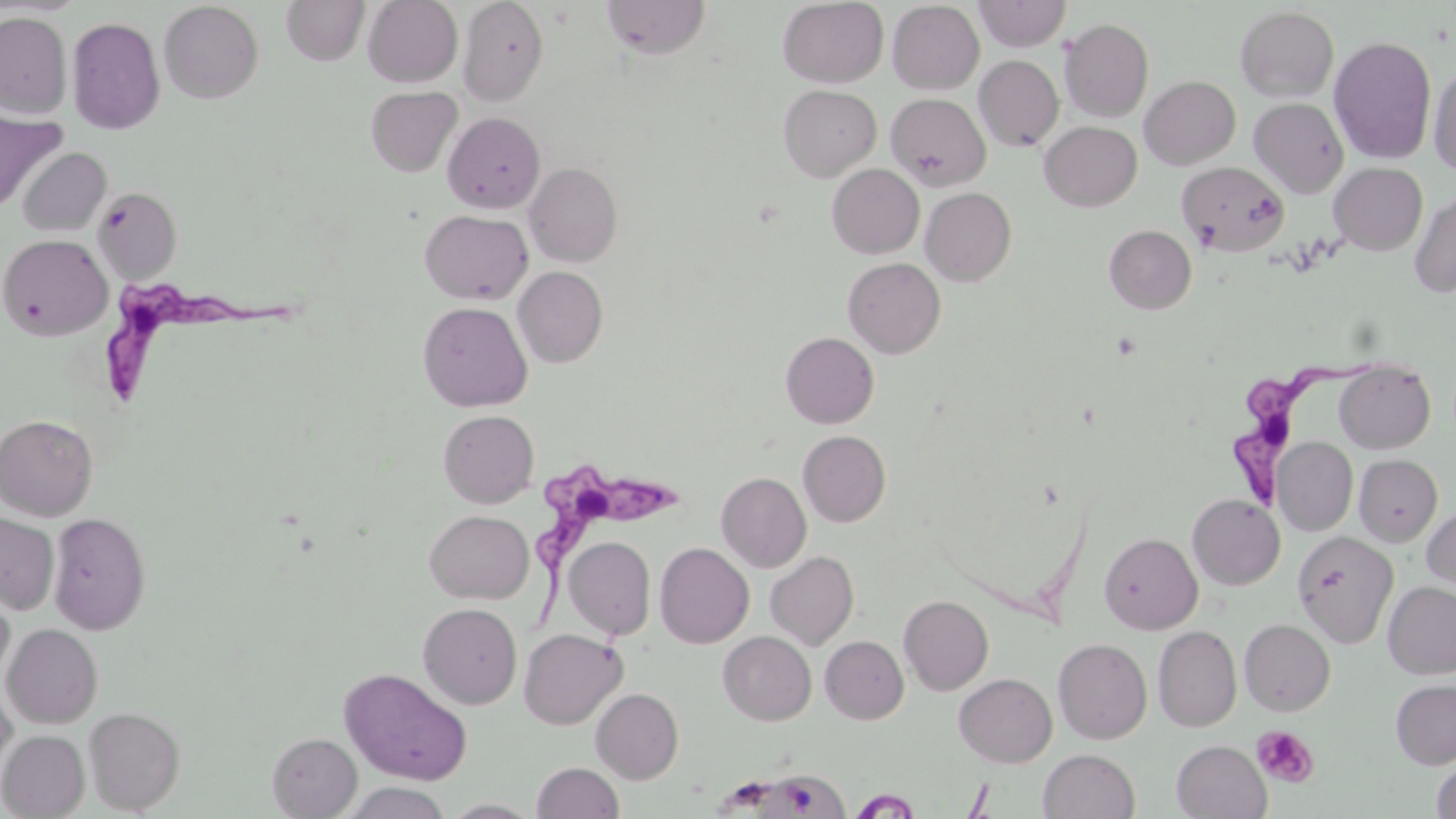
slide-level diagnosis = Trypanosoma brucei
magnification = 1000x
uninfected red blood cell locations = approximate bounding boxes as (x1,y1)-(x2,y2) corner pairs in pixels: (281,0)-(370,66), (363,0)-(463,87), (457,0)-(548,107), (601,0)-(710,59), (777,0)-(889,88), (974,0)-(1071,51), (159,1)-(264,103), (887,1)-(985,94), (1235,5)-(1339,103), (66,10)-(262,118), (0,12)-(72,118), (66,17)-(166,134), (1060,18)-(1154,123), (1328,36)-(1437,164), (974,55)-(1064,152), (1428,61)-(1456,177), (1140,75)-(1240,169), (778,85)-(881,182), (365,86)-(462,177), (886,93)-(991,190), (1249,97)-(1349,198), (0,109)-(66,212), (443,112)-(545,213), (1039,121)-(1142,211), (18,147)-(111,236), (1177,161)-(1289,255), (524,162)-(623,267), (1329,162)-(1428,255), (827,164)-(924,258), (93,187)-(182,282), (921,187)-(1016,286), (1410,189)-(1456,298), (420,210)-(533,304), (1104,225)-(1197,314), (1,233)-(113,340), (843,257)-(945,358), (514,266)-(609,367), (418,301)-(532,412), (781,332)-(879,428), (1334,360)-(1435,454), (438,409)-(539,508), (0,414)-(98,520), (798,430)-(891,527), (1273,437)-(1358,536), (1354,455)-(1443,546), (716,472)-(811,572), (1187,494)-(1285,590), (1422,504)-(1456,595), (424,510)-(534,604), (48,512)-(151,635), (0,514)-(59,614), (1293,531)-(1398,647), (1099,532)-(1203,635), (564,536)-(656,640), (654,542)-(754,648), (765,551)-(859,650), (1383,582)-(1456,679), (0,588)-(15,688), (899,595)-(993,695), (418,603)-(522,709), (1239,619)-(1335,716), (2,624)-(103,728), (1153,626)-(1242,731), (519,628)-(627,729), (718,631)-(816,725), (820,636)-(909,724), (1053,638)-(1152,744), (338,666)-(473,785), (954,673)-(1057,767), (1390,679)-(1456,769), (0,680)-(17,781), (590,688)-(684,784), (84,706)-(185,814), (0,730)-(89,818), (267,732)-(362,818), (1172,740)-(1271,818), (1039,749)-(1140,819), (1431,760)-(1456,818), (532,762)-(623,819), (760,770)-(855,819), (341,782)-(452,819), (849,788)-(923,817), (441,799)-(542,818)
Trypanosoma brucei locations = approximate bounding boxes as (x1,y1)-(x2,y2) corner pairs in pixels: (106,271)-(311,403), (1224,352)-(1370,513), (539,459)-(684,616)
modality = optical microscopy
image size = 1456×819 pixels
field of view = one of a larger specimen
platelet locations = approximate bounding boxes as (x1,y1)-(x2,y2) corner pairs in pixels: (1251,725)-(1319,787)
stain = May-Grünwald-Giemsa
preparation = thin blood smear